Find the red blood cells and label each as P. falciparum-infected, uninfected, or of indeterminate infection status.
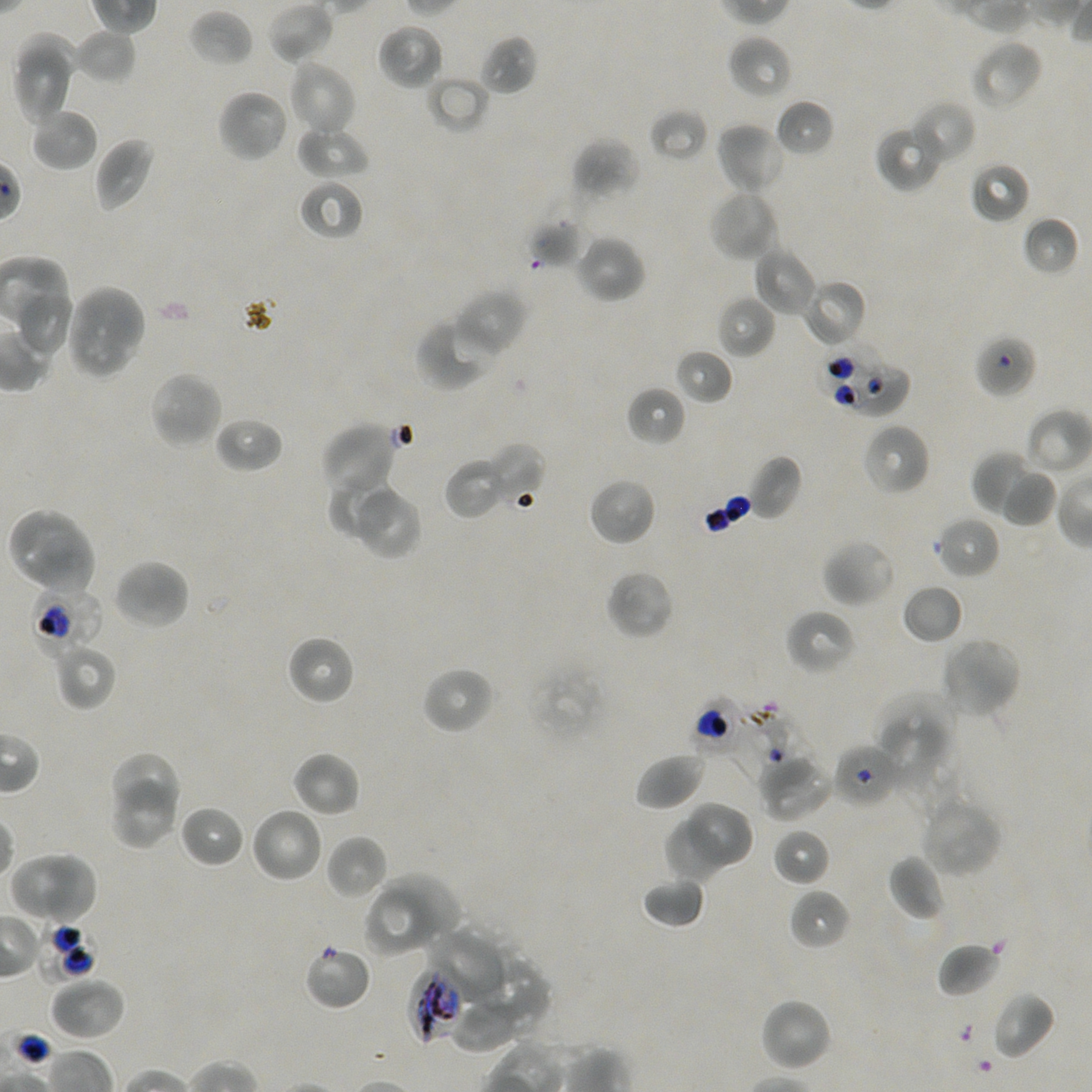

Approximate bounding boxes as (x1, y1, x2, y2) in pixels. Not every red blood cell is marked.
Red blood cells of indeterminate infection status: (974, 333, 1036, 399), (817, 347, 890, 405), (854, 365, 912, 418), (30, 585, 105, 654), (691, 696, 748, 754), (733, 702, 807, 780), (833, 742, 902, 809), (36, 919, 98, 983), (304, 944, 371, 1011), (408, 964, 468, 1046).
Uninfected red blood cells: (267, 1, 335, 65), (188, 9, 253, 67), (378, 22, 444, 90), (72, 28, 137, 84), (11, 31, 84, 84), (480, 34, 538, 96), (728, 35, 793, 100), (970, 37, 1044, 111), (14, 52, 77, 125), (287, 58, 357, 138), (425, 75, 488, 135), (217, 88, 290, 163), (775, 98, 835, 158), (909, 100, 975, 166), (29, 107, 99, 171), (649, 107, 708, 163), (296, 122, 371, 179), (716, 122, 786, 195), (876, 124, 943, 192), (94, 137, 157, 213), (572, 139, 639, 202), (969, 161, 1031, 224), (297, 178, 364, 241), (708, 188, 780, 262), (528, 211, 589, 269), (1021, 216, 1078, 278), (575, 234, 646, 304), (752, 245, 816, 317), (800, 278, 867, 348), (65, 284, 147, 380), (14, 289, 75, 358), (452, 289, 528, 357), (716, 295, 775, 359), (416, 316, 496, 392), (674, 349, 733, 405), (148, 371, 223, 450), (625, 386, 686, 446), (1027, 407, 1092, 475), (215, 416, 284, 474), (321, 422, 401, 499), (862, 422, 930, 496), (484, 442, 545, 507), (972, 451, 1048, 522), (747, 456, 802, 520), (444, 457, 507, 520), (998, 470, 1057, 528), (327, 473, 400, 541), (588, 477, 657, 546), (349, 482, 423, 560), (6, 507, 96, 596), (934, 515, 1001, 580), (822, 538, 897, 608), (112, 558, 191, 632), (606, 569, 674, 640), (901, 583, 964, 644), (785, 608, 858, 676), (286, 635, 356, 706), (940, 637, 1023, 721), (52, 642, 116, 710), (420, 666, 496, 735), (873, 692, 956, 771), (875, 715, 943, 790), (107, 750, 185, 809), (291, 750, 361, 817), (634, 752, 706, 812), (758, 754, 834, 821), (109, 778, 181, 848), (920, 794, 1004, 878), (687, 799, 754, 871), (179, 805, 246, 868), (249, 806, 324, 884), (667, 818, 726, 881), (771, 828, 831, 887), (325, 835, 388, 902), (9, 851, 99, 926), (887, 853, 945, 922), (377, 869, 462, 939), (641, 877, 706, 929), (788, 888, 851, 951), (365, 891, 439, 956), (424, 924, 510, 1003), (937, 941, 1002, 998), (472, 954, 549, 1036), (49, 976, 126, 1041), (991, 991, 1055, 1060), (759, 997, 834, 1072), (452, 1002, 513, 1055).
No infected red blood cells observed.

Summary:
  - Preparation: thin blood film
  - Culture: static in-vitro P. falciparum strain NF54
  - Image size: 1092×1092 pixels
  - Donor blood group: A+/O+
  - Field of view: one from this slide
  - Stain: Giemsa
  - Objective: 100x, oil immersion, numerical aperture 1.45